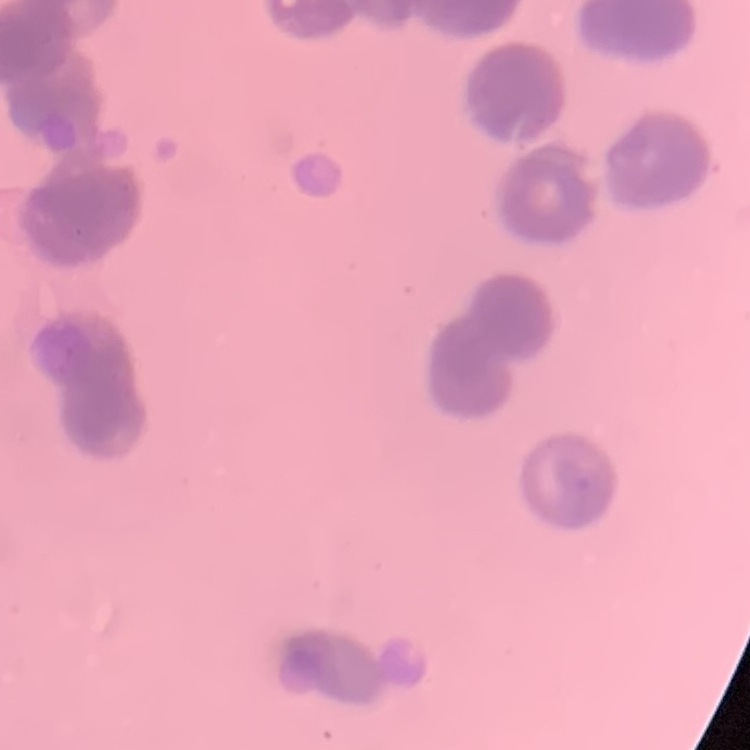
Summary:
  - Erythrocyte morphology: rouleaux formation
  - Image type: square crop of a larger photomicrograph
  - Preparation: thin blood film
  - Stain: Field's or Giemsa